Classify this cell by malaria status.
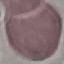
Uninfected.

Giemsa stain. Thin blood smear. Photographed with a smartphone camera at the microscope eyepiece. Automatically extracted cell patch, resized to 64 × 64 pixels.